Classify this cell by malaria status.
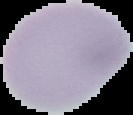

It is uninfected.

Image is 133×115 pixels. From a thin blood smear. Segmented cell region on a black background.